Point out every malaria parasite and every leukocyte.
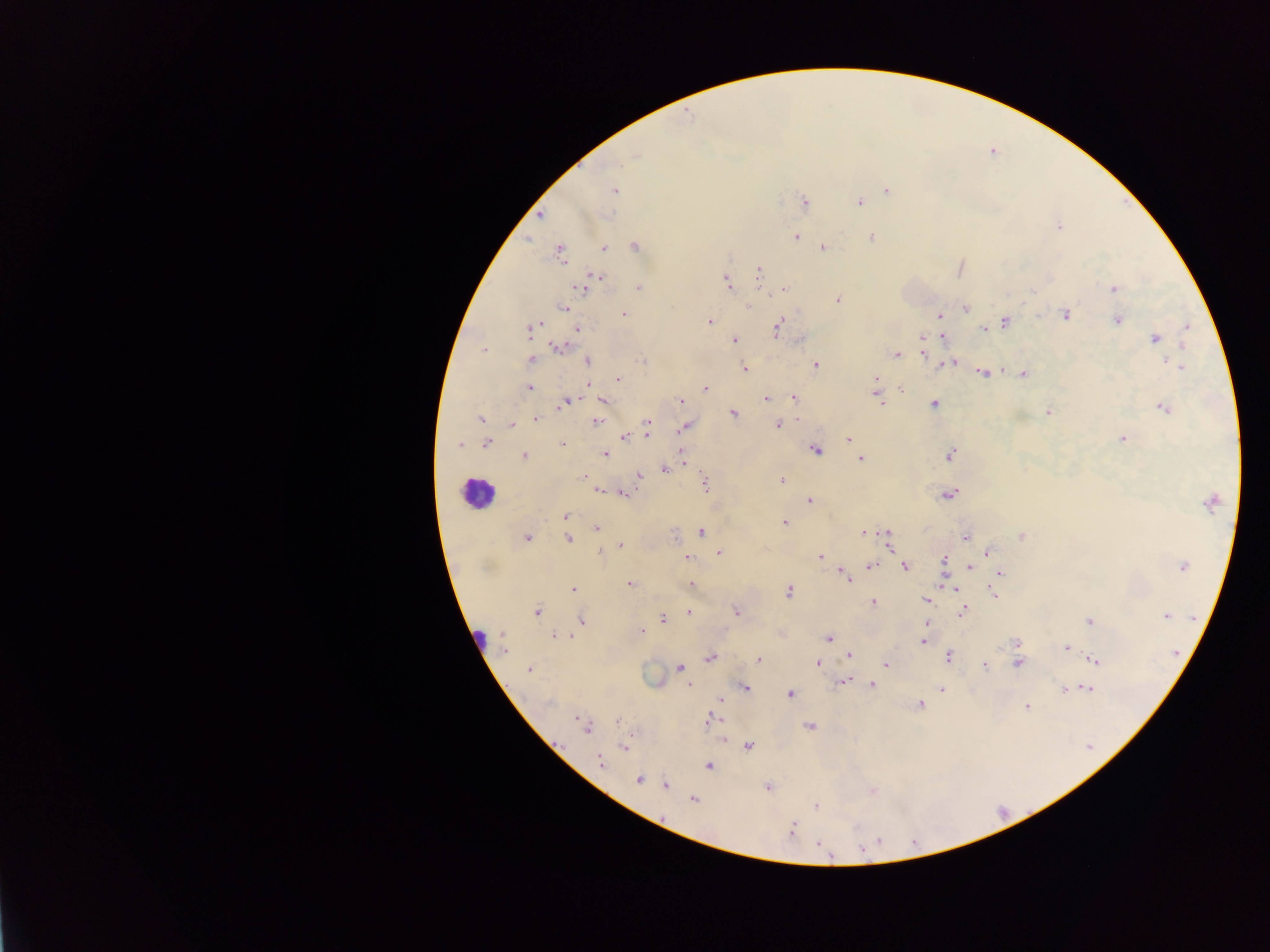
Approximate centers as [x, y] in pixels.
Malaria parasites: [636, 156], [621, 163], [886, 191], [614, 192], [803, 201], [859, 201], [1057, 228], [797, 237], [871, 238], [634, 246], [823, 247], [604, 248], [559, 252], [758, 272], [596, 275], [727, 282], [579, 288], [638, 288], [1115, 289], [783, 290], [836, 297], [750, 307], [965, 307], [565, 308], [623, 313], [939, 314], [1066, 315], [1005, 321], [1116, 321], [710, 322], [776, 328], [576, 329], [526, 330], [984, 330], [942, 336], [734, 339], [1154, 339], [1182, 342], [558, 348], [923, 352], [483, 353], [896, 354], [916, 355], [588, 359], [531, 360], [643, 361], [953, 363], [815, 364], [943, 364], [949, 364], [1173, 364], [744, 368], [983, 372], [1022, 373], [618, 378], [902, 387], [529, 388], [705, 388], [793, 397], [603, 399], [880, 399], [765, 400], [571, 401], [680, 401], [564, 402], [933, 403], [1164, 409], [733, 413], [1048, 414], [480, 418], [536, 418], [798, 418], [512, 423], [594, 423], [778, 425], [683, 429], [646, 433], [623, 438], [1121, 438], [848, 439], [486, 442], [459, 444], [563, 444], [681, 451], [817, 452], [948, 454], [524, 455], [606, 455], [861, 457], [685, 462], [663, 470], [582, 476], [638, 476], [782, 480], [703, 482], [598, 488], [623, 493], [947, 496], [809, 501], [1207, 503], [565, 516], [784, 522], [597, 527], [701, 532], [528, 535], [863, 535], [1020, 535], [964, 536], [568, 538], [622, 543], [890, 544], [719, 551], [986, 551], [600, 552], [821, 555], [687, 558], [944, 560], [872, 566], [1182, 566], [905, 567], [971, 567], [999, 573], [842, 574], [847, 578], [629, 583], [692, 583], [575, 590], [955, 590], [788, 591], [995, 596], [925, 600], [874, 602], [736, 611], [963, 611], [536, 612], [687, 613], [1165, 616], [582, 619], [662, 619], [1088, 621], [642, 629], [502, 634], [552, 635], [829, 638], [925, 641], [1017, 643], [503, 648], [1066, 648], [849, 655], [948, 656], [757, 659], [1096, 660], [708, 662], [817, 663], [884, 663], [1019, 664], [984, 667], [678, 668], [529, 671], [845, 680], [874, 685], [688, 686], [747, 688], [941, 688], [1087, 688], [1064, 690], [790, 693], [720, 700], [919, 704], [1026, 706], [709, 717], [576, 720], [618, 721], [810, 726], [588, 730], [722, 741], [748, 746], [623, 747], [599, 762], [709, 766], [639, 779], [665, 786], [766, 788], [691, 799], [814, 805], [792, 827], [817, 843].
Leukocytes: [478, 491].

Image is 1270×952 pixels. Thick blood film. Mobile-phone photograph taken through the microscope. Sample from Ghana. One field of view.